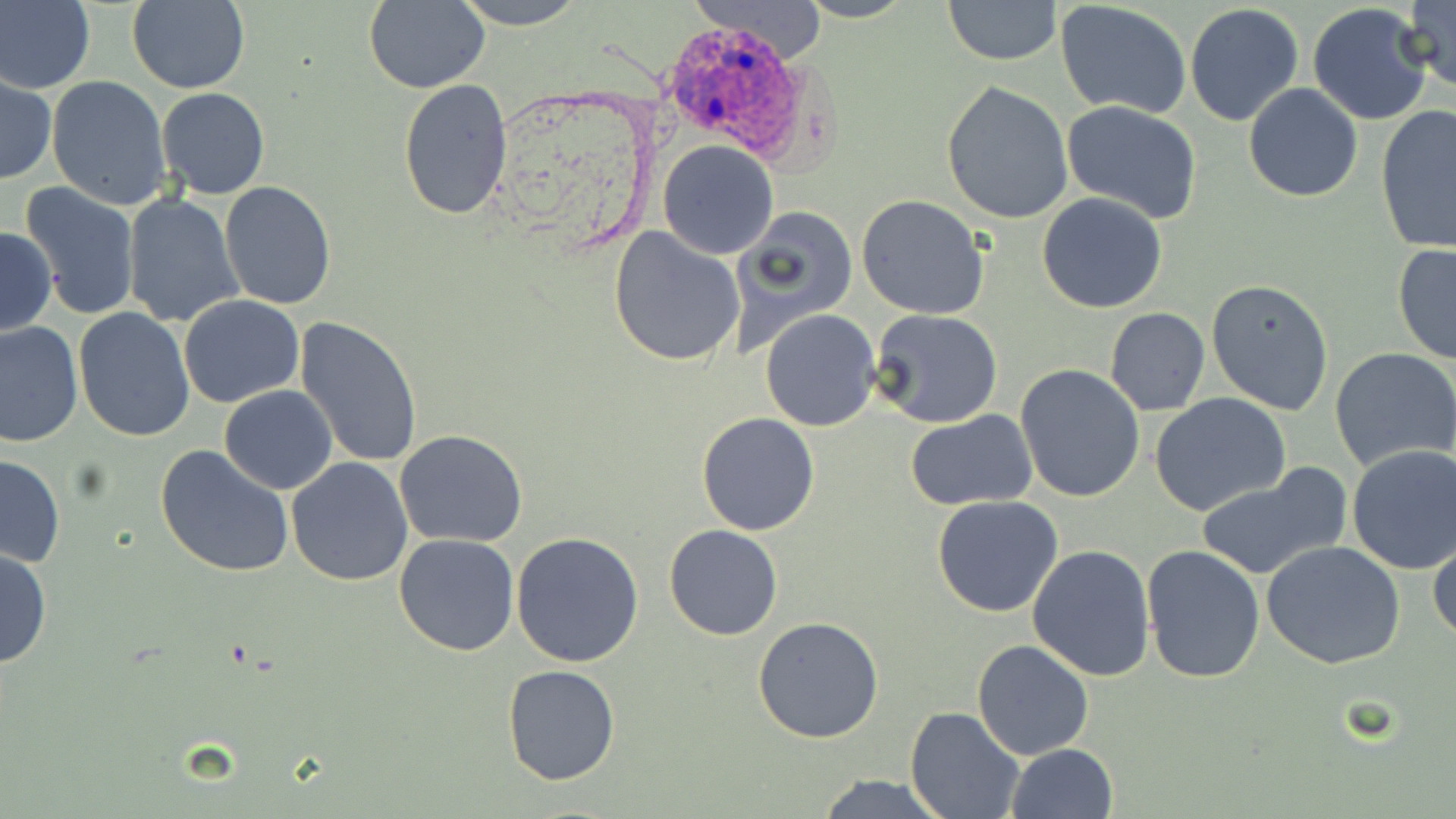

{
  "slide_level_diagnosis": "Plasmodium ovale",
  "image_size": "1456×819 pixels",
  "modality": "light microscopy",
  "field_of_view": "one of a larger specimen",
  "stain": "May-Grünwald-Giemsa",
  "preparation": "thin blood film",
  "plasmodium_ovale_infected_red_blood_cell_locations": "approximate bounding boxes as named x1/y1/x2/y2 corners in pixels: (x1=656, y1=15, x2=806, y2=159)",
  "magnification": "1000x",
  "uninfected_red_blood_cell_locations": "approximate bounding boxes as named x1/y1/x2/y2 corners in pixels: (x1=0, y1=0, x2=95, y2=95), (x1=449, y1=0, x2=588, y2=29), (x1=795, y1=0, x2=917, y2=22), (x1=942, y1=0, x2=1061, y2=65), (x1=1400, y1=0, x2=1456, y2=92), (x1=126, y1=1, x2=250, y2=93), (x1=363, y1=1, x2=491, y2=94), (x1=682, y1=1, x2=831, y2=62), (x1=1055, y1=1, x2=1193, y2=117), (x1=1307, y1=1, x2=1435, y2=126), (x1=1184, y1=3, x2=1305, y2=128), (x1=1, y1=74, x2=56, y2=186), (x1=46, y1=75, x2=172, y2=211), (x1=398, y1=78, x2=514, y2=221), (x1=940, y1=80, x2=1075, y2=224), (x1=1243, y1=83, x2=1363, y2=203), (x1=157, y1=87, x2=270, y2=201), (x1=1060, y1=101, x2=1204, y2=225), (x1=1375, y1=105, x2=1456, y2=256), (x1=658, y1=140, x2=780, y2=259), (x1=220, y1=182, x2=336, y2=311), (x1=19, y1=183, x2=142, y2=321), (x1=121, y1=192, x2=245, y2=327), (x1=1037, y1=192, x2=1168, y2=314), (x1=856, y1=194, x2=991, y2=319), (x1=728, y1=209, x2=859, y2=352), (x1=609, y1=225, x2=745, y2=369), (x1=1, y1=227, x2=57, y2=336), (x1=1393, y1=243, x2=1456, y2=369), (x1=1205, y1=278, x2=1334, y2=416), (x1=178, y1=295, x2=305, y2=407), (x1=74, y1=308, x2=196, y2=444), (x1=1103, y1=308, x2=1210, y2=415), (x1=869, y1=310, x2=1003, y2=429), (x1=758, y1=311, x2=881, y2=431), (x1=293, y1=317, x2=424, y2=471), (x1=0, y1=322, x2=83, y2=449), (x1=1330, y1=346, x2=1456, y2=472), (x1=1016, y1=364, x2=1147, y2=503), (x1=219, y1=385, x2=339, y2=494), (x1=1151, y1=394, x2=1291, y2=517), (x1=696, y1=411, x2=820, y2=536), (x1=906, y1=411, x2=1037, y2=509), (x1=394, y1=429, x2=527, y2=548), (x1=153, y1=443, x2=297, y2=580), (x1=1347, y1=445, x2=1456, y2=575), (x1=1, y1=453, x2=67, y2=568), (x1=285, y1=457, x2=413, y2=587), (x1=1198, y1=464, x2=1353, y2=581), (x1=932, y1=495, x2=1063, y2=617), (x1=664, y1=524, x2=782, y2=642), (x1=510, y1=531, x2=645, y2=668), (x1=1428, y1=532, x2=1456, y2=644), (x1=393, y1=533, x2=520, y2=656), (x1=1262, y1=540, x2=1405, y2=668), (x1=0, y1=542, x2=52, y2=671), (x1=1027, y1=544, x2=1156, y2=682), (x1=1141, y1=545, x2=1267, y2=684), (x1=752, y1=615, x2=884, y2=742), (x1=970, y1=639, x2=1095, y2=760), (x1=502, y1=665, x2=620, y2=785), (x1=906, y1=708, x2=1025, y2=819), (x1=1006, y1=743, x2=1119, y2=819), (x1=817, y1=773, x2=951, y2=818)"
}